Report the malaria status of this cell.
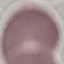
Uninfected.

capture: smartphone camera at the microscope eyepiece
image_type: automatically extracted cell patch, resized to 64 × 64 pixels
stain: Giemsa
preparation: thin blood film